Name the parasite shown.
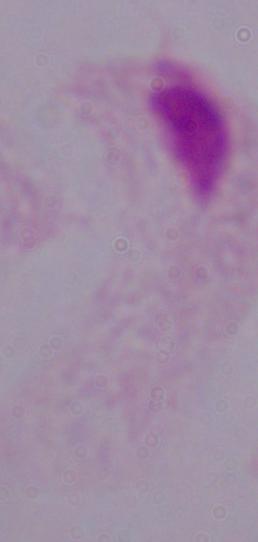

A trichomonad.

Summary:
  - Magnification: 1000x
  - Modality: photomicrograph